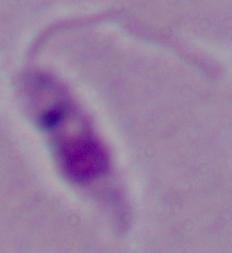

modality = photomicrograph
magnification = 1000x
identification = Leishmania